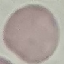
Malaria status: uninfected. Acquired by smartphone through the microscope eyepiece. Giemsa stain. Thin smear of blood. Cell patch, automatically extracted from a larger field of view and resized to 64 × 64 pixels.